Evaluate for malaria.
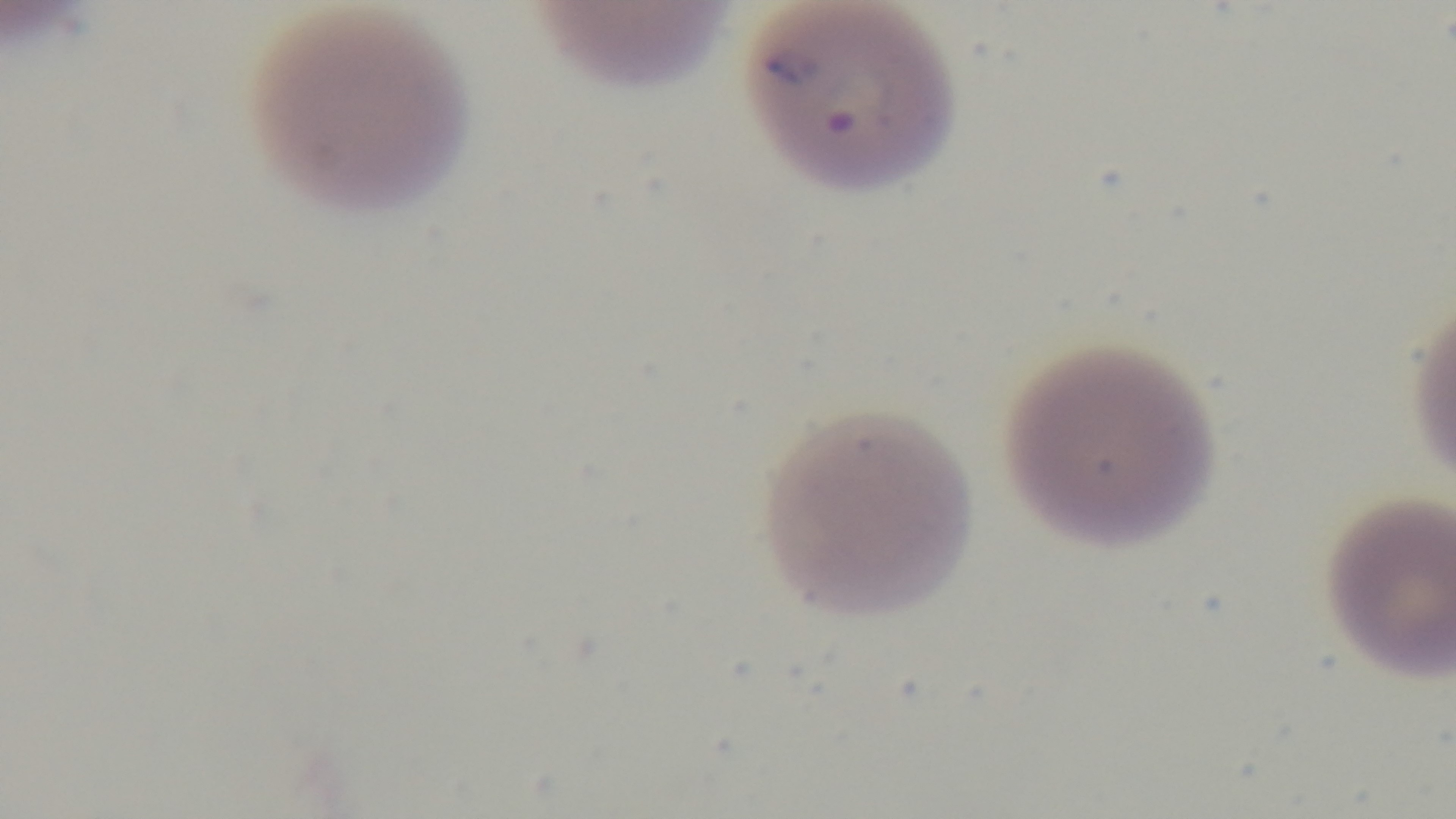
Infected.

Summary:
  - Preparation: thin blood film
  - Capture: mounted 4K digital camera
  - Modality: light microscopy
  - Field of view: single
  - Objective: 100x oil immersion
  - Stain: Giemsa